Give the preparation type.
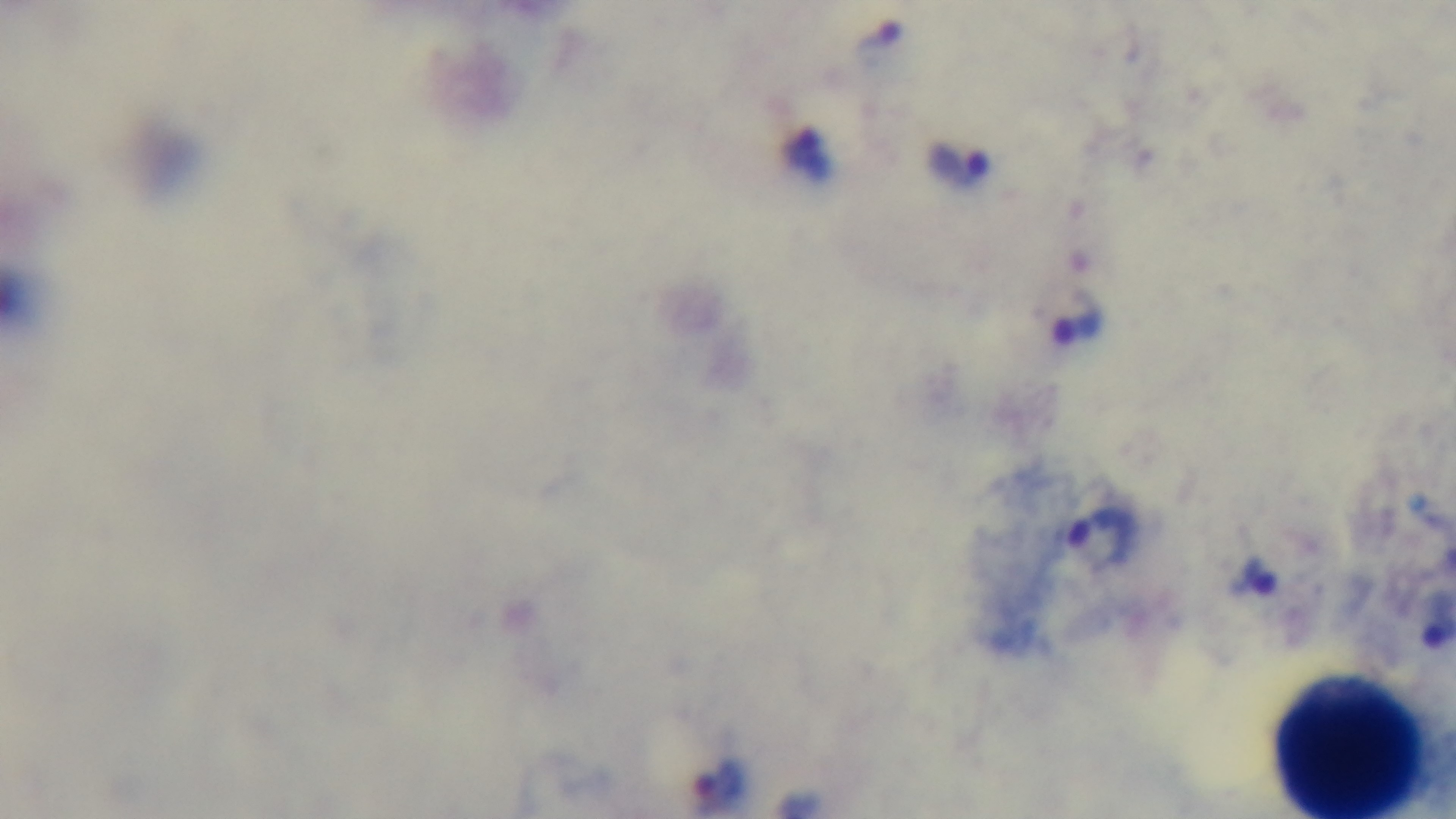

Thick.

modality = light microscopy
stain = Giemsa
objective = 100x oil immersion
capture = mounted 4K digital camera
field of view = one from the slide
malaria status = infected